State which cell type is depicted.
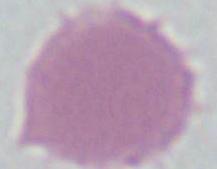
This is an erythrocyte.

magnification = 1000x
modality = photomicrograph